Report the malaria status.
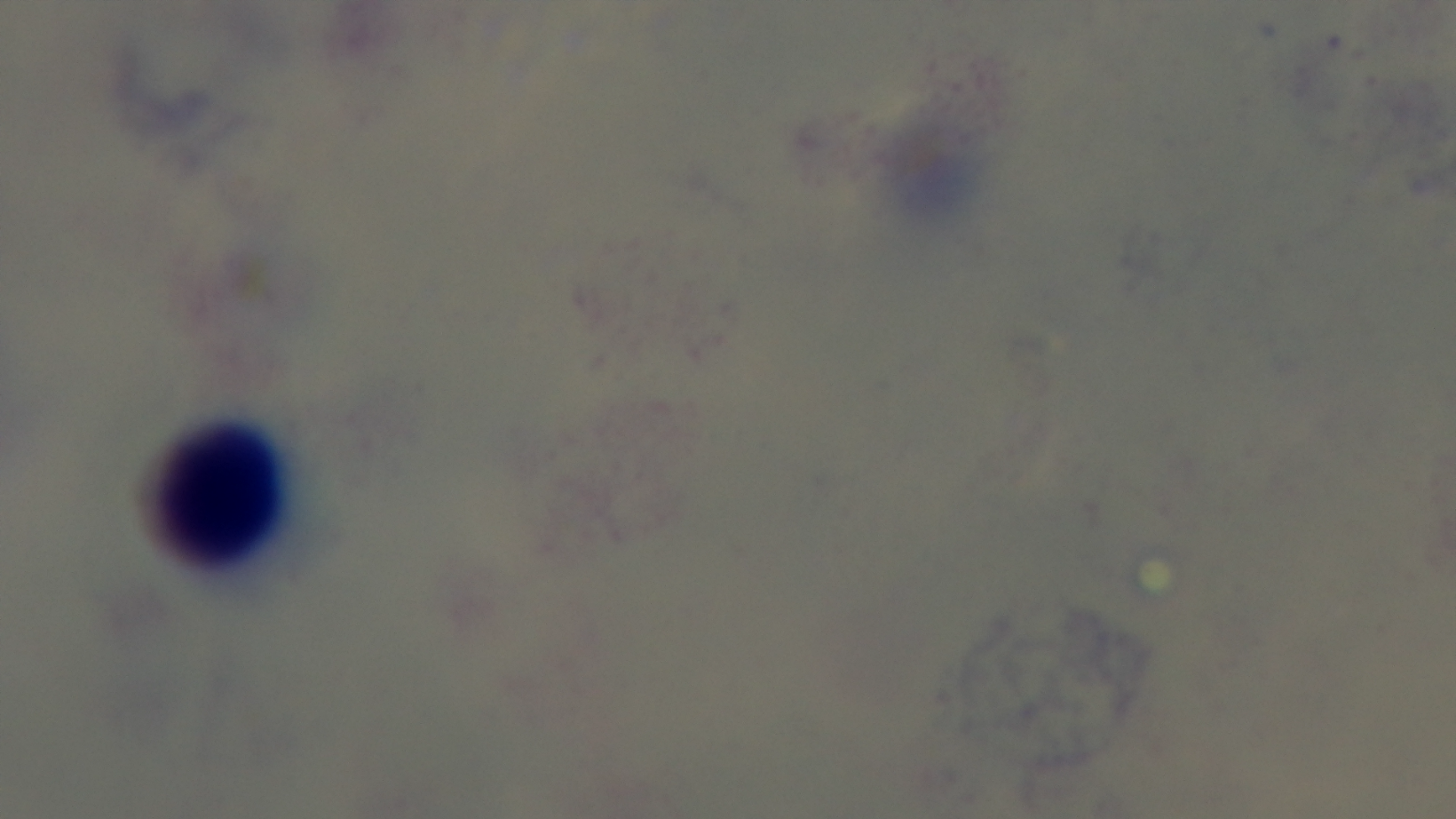
It is uninfected.

capture: mounted 4K digital camera
modality: light microscopy
preparation: thick blood film
stain: Giemsa
field_of_view: one from the slide
objective: 100x oil immersion